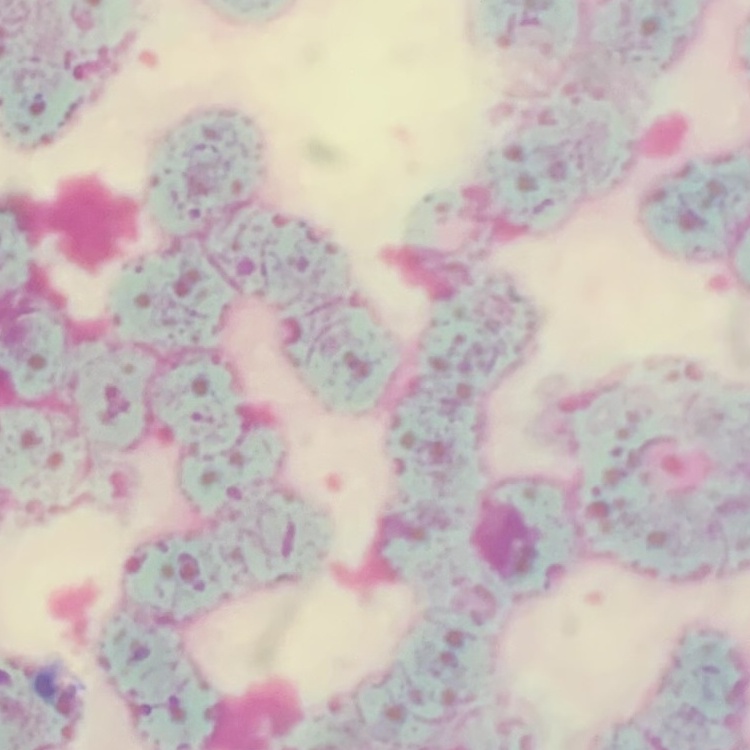

{
  "erythrocyte_morphology": "rouleaux formation",
  "stain": "Field's or Giemsa",
  "image_type": "square crop of a larger photomicrograph",
  "preparation": "thin blood smear"
}